State which parasite is depicted.
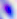
Toxoplasma gondii.

Summary:
  - Magnification: 400x
  - Modality: photomicrograph